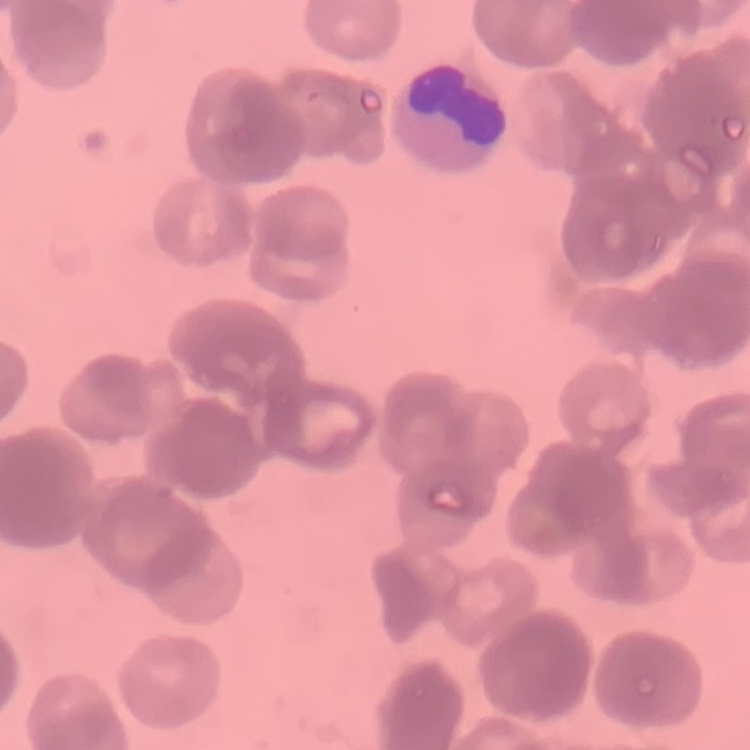

The erythrocytes exhibit rouleaux formation. Thin peripheral smear. Field's or Giemsa stain. Square crop of a larger photomicrograph.